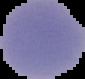

malaria status = uninfected
preparation = thin blood film
image type = segmented cell region on a black background
image size = 85×79 pixels